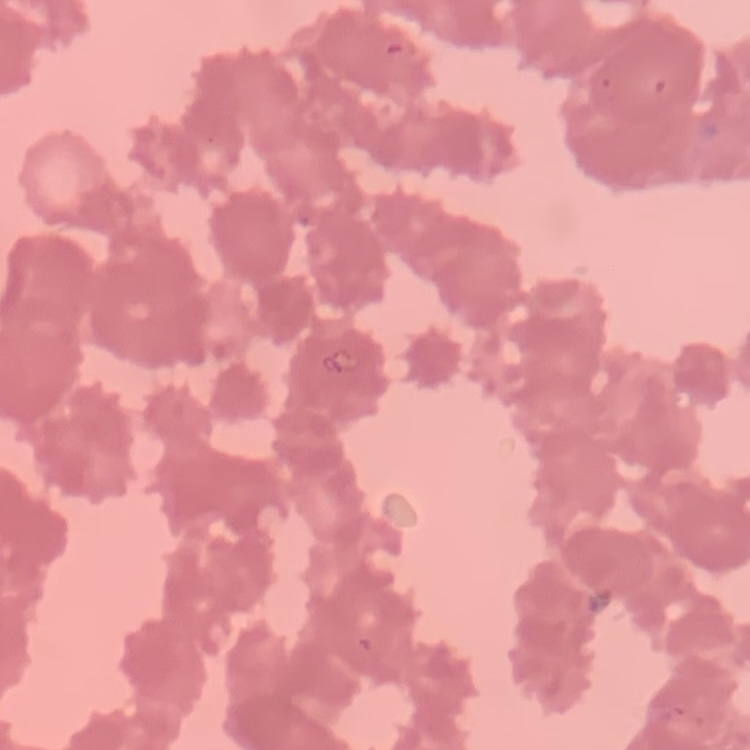

The erythrocytes exhibit rouleaux formation. Thin peripheral smear. Square crop of a larger photomicrograph. Field's or Giemsa stain.